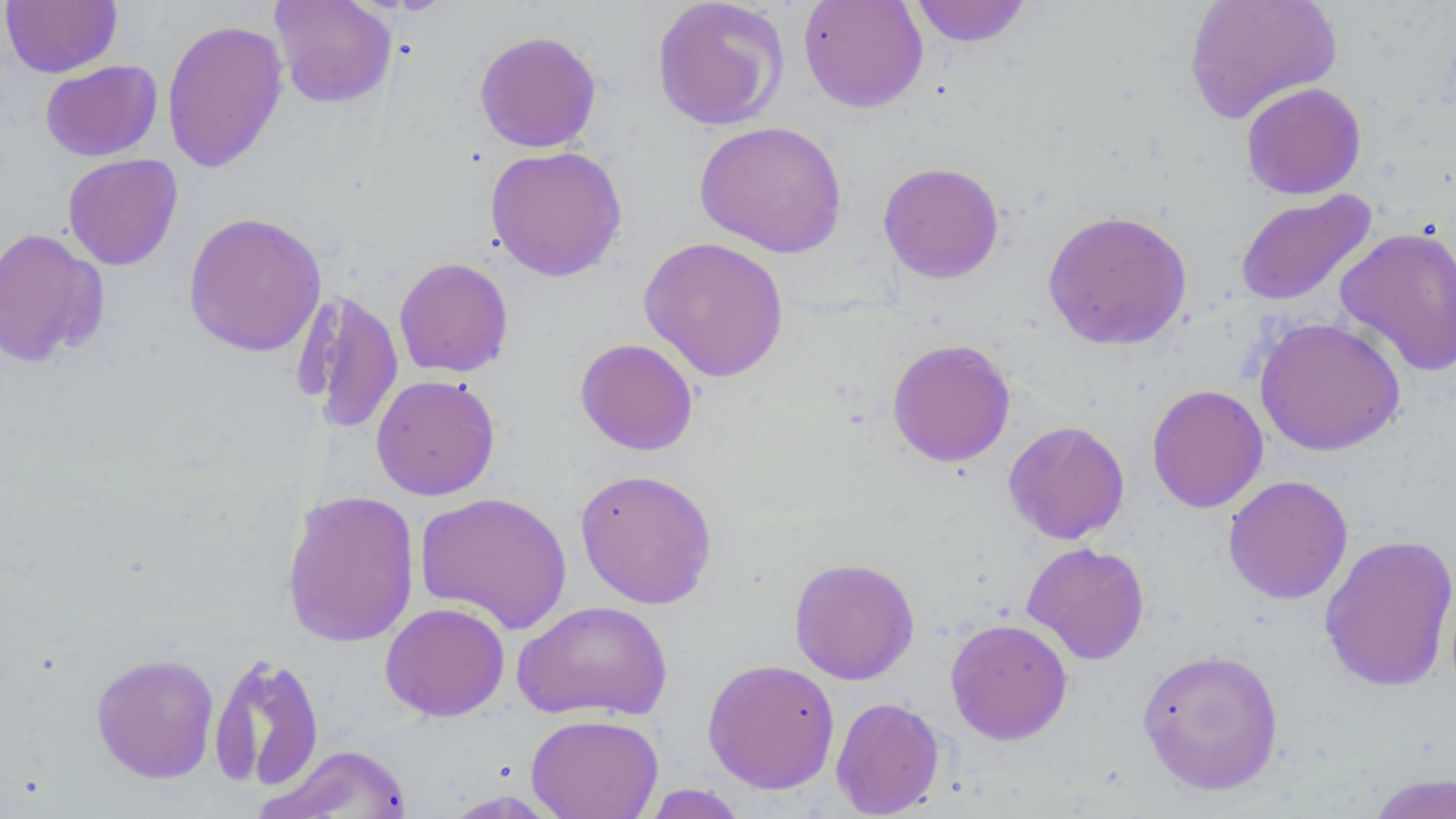
Summary:
  - Coordinate format: approximate bounding boxes as (x1,y1)-(x2,y2) corner pairs in pixels
  - Uninfected red blood cell locations: (270,0)-(397,108), (651,0)-(789,131), (798,0)-(928,113), (909,0)-(1033,47), (1183,0)-(1342,123), (1,1)-(122,77), (161,19)-(289,173), (474,30)-(602,153), (40,60)-(162,161), (1241,82)-(1366,199), (694,120)-(847,258), (485,145)-(627,282), (62,154)-(183,270), (878,161)-(1004,284), (1234,189)-(1378,307), (1042,208)-(1193,351), (183,211)-(327,357), (1334,225)-(1456,377), (0,228)-(109,368), (639,236)-(790,382), (394,257)-(514,378), (294,290)-(403,436), (1254,316)-(1406,456), (575,338)-(699,456), (887,338)-(1015,468), (370,374)-(501,500), (1146,384)-(1269,513), (1003,420)-(1130,544), (575,468)-(717,609), (1223,475)-(1353,604), (281,488)-(420,649), (415,490)-(572,633), (1319,533)-(1456,693), (1021,541)-(1150,665), (789,557)-(920,685), (512,600)-(673,722), (380,602)-(510,721), (945,618)-(1073,745), (1137,647)-(1284,797), (207,652)-(326,793), (91,653)-(220,783), (702,658)-(840,794), (830,696)-(945,817), (526,713)-(664,819), (261,743)-(415,819), (1364,772)-(1456,818), (639,783)-(750,818), (441,791)-(564,818)
  - Slide-level diagnosis: no evidence of blood parasites
  - Stain: May-Grünwald-Giemsa
  - Magnification: 1000x
  - Field of view: one of a larger specimen
  - Image size: 1456×819 pixels
  - Modality: light microscopy
  - Preparation: thin blood film